Identify the parasite.
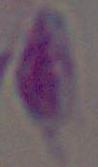

This is Toxoplasma gondii.

Captured at 1000x magnification. Photomicrograph.